Name the parasite shown.
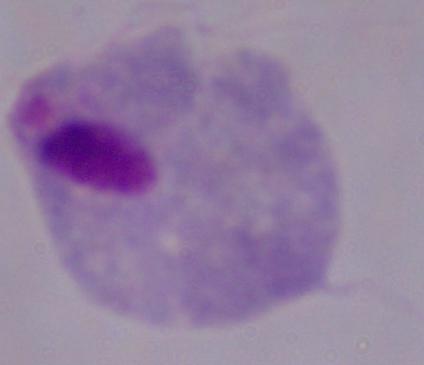

A trichomonad.

modality: micrograph
magnification: 1000x